Report the malaria status of this cell.
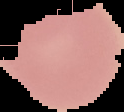

It is uninfected.

Image is 124×112 pixels. Segmented cell region on a black background. From a thin blood film.